Give the extent of all Trypanosoma brucei.
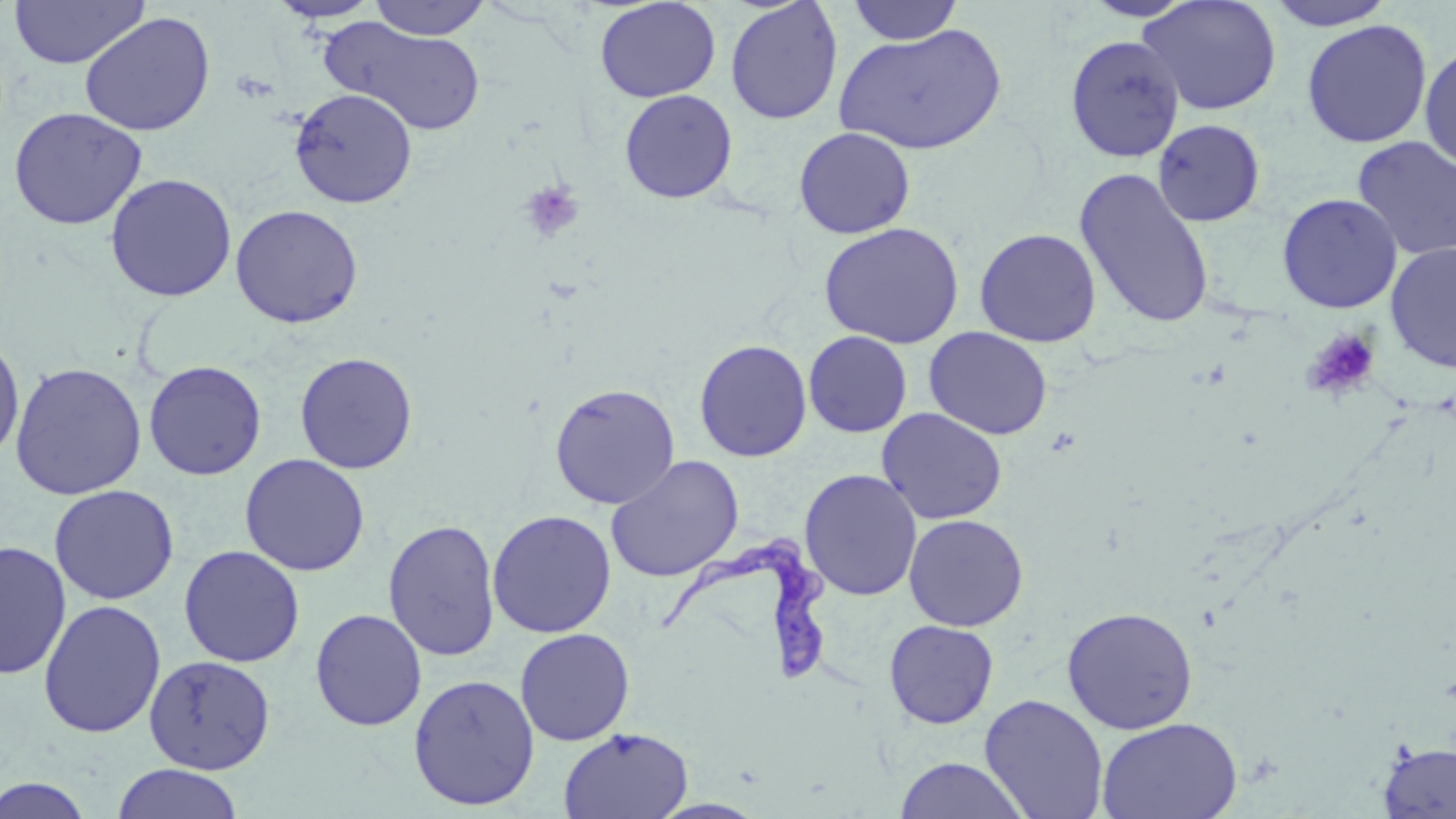
Approximate bounding boxes as named x1/y1/x2/y2 corners in pixels.
Trypanosoma brucei: (x1=657, y1=535, x2=832, y2=688).

slide-level diagnosis = Trypanosoma brucei
modality = light microscopy
field of view = single
platelet locations = approximate bounding boxes as named x1/y1/x2/y2 corners in pixels: (x1=518, y1=179, x2=585, y2=244), (x1=1303, y1=327, x2=1381, y2=401)
image size = 1456×819 pixels
preparation = thin blood smear
magnification = 1000x
stain = May-Grünwald-Giemsa
uninfected red blood cell locations = approximate bounding boxes as named x1/y1/x2/y2 corners in pixels: (x1=8, y1=0, x2=148, y2=68), (x1=267, y1=0, x2=383, y2=22), (x1=368, y1=0, x2=492, y2=40), (x1=594, y1=0, x2=720, y2=103), (x1=725, y1=0, x2=843, y2=125), (x1=1080, y1=0, x2=1199, y2=21), (x1=1137, y1=0, x2=1282, y2=115), (x1=1263, y1=0, x2=1399, y2=31), (x1=846, y1=1, x2=964, y2=45), (x1=79, y1=12, x2=216, y2=136), (x1=322, y1=18, x2=487, y2=136), (x1=1302, y1=19, x2=1432, y2=149), (x1=834, y1=23, x2=1007, y2=156), (x1=1065, y1=35, x2=1186, y2=162), (x1=1419, y1=42, x2=1455, y2=174), (x1=289, y1=88, x2=417, y2=208), (x1=619, y1=90, x2=737, y2=203), (x1=8, y1=106, x2=147, y2=230), (x1=1152, y1=119, x2=1266, y2=226), (x1=793, y1=127, x2=915, y2=239), (x1=1352, y1=136, x2=1456, y2=260), (x1=1074, y1=168, x2=1216, y2=330), (x1=105, y1=173, x2=237, y2=302), (x1=1277, y1=193, x2=1403, y2=314), (x1=230, y1=204, x2=364, y2=328), (x1=818, y1=222, x2=964, y2=349), (x1=974, y1=228, x2=1101, y2=347), (x1=1385, y1=243, x2=1456, y2=373), (x1=924, y1=327, x2=1053, y2=440), (x1=803, y1=331, x2=912, y2=437), (x1=0, y1=333, x2=25, y2=463), (x1=694, y1=339, x2=812, y2=462), (x1=295, y1=352, x2=418, y2=474), (x1=143, y1=360, x2=267, y2=480), (x1=9, y1=361, x2=147, y2=500), (x1=549, y1=383, x2=680, y2=509), (x1=877, y1=408, x2=1008, y2=524), (x1=239, y1=453, x2=370, y2=576), (x1=606, y1=455, x2=744, y2=582), (x1=799, y1=469, x2=922, y2=601), (x1=48, y1=484, x2=179, y2=605), (x1=487, y1=510, x2=616, y2=638), (x1=903, y1=514, x2=1029, y2=632), (x1=383, y1=518, x2=501, y2=662), (x1=0, y1=540, x2=71, y2=679), (x1=178, y1=545, x2=305, y2=667), (x1=38, y1=599, x2=166, y2=739), (x1=1061, y1=606, x2=1199, y2=734), (x1=310, y1=608, x2=427, y2=731), (x1=884, y1=620, x2=999, y2=729), (x1=515, y1=628, x2=635, y2=745), (x1=144, y1=654, x2=275, y2=773), (x1=408, y1=674, x2=540, y2=810), (x1=980, y1=694, x2=1108, y2=818), (x1=1097, y1=716, x2=1242, y2=819), (x1=558, y1=727, x2=693, y2=819), (x1=1377, y1=741, x2=1456, y2=818), (x1=894, y1=756, x2=1029, y2=819), (x1=111, y1=763, x2=243, y2=819), (x1=0, y1=775, x2=95, y2=818)